Classify this cell by malaria status.
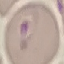
Parasitized.

{
  "image_type": "automatically extracted cell patch, resized to 64 × 64 pixels",
  "capture": "smartphone through the microscope eyepiece",
  "preparation": "thin blood film",
  "stain": "Giemsa"
}